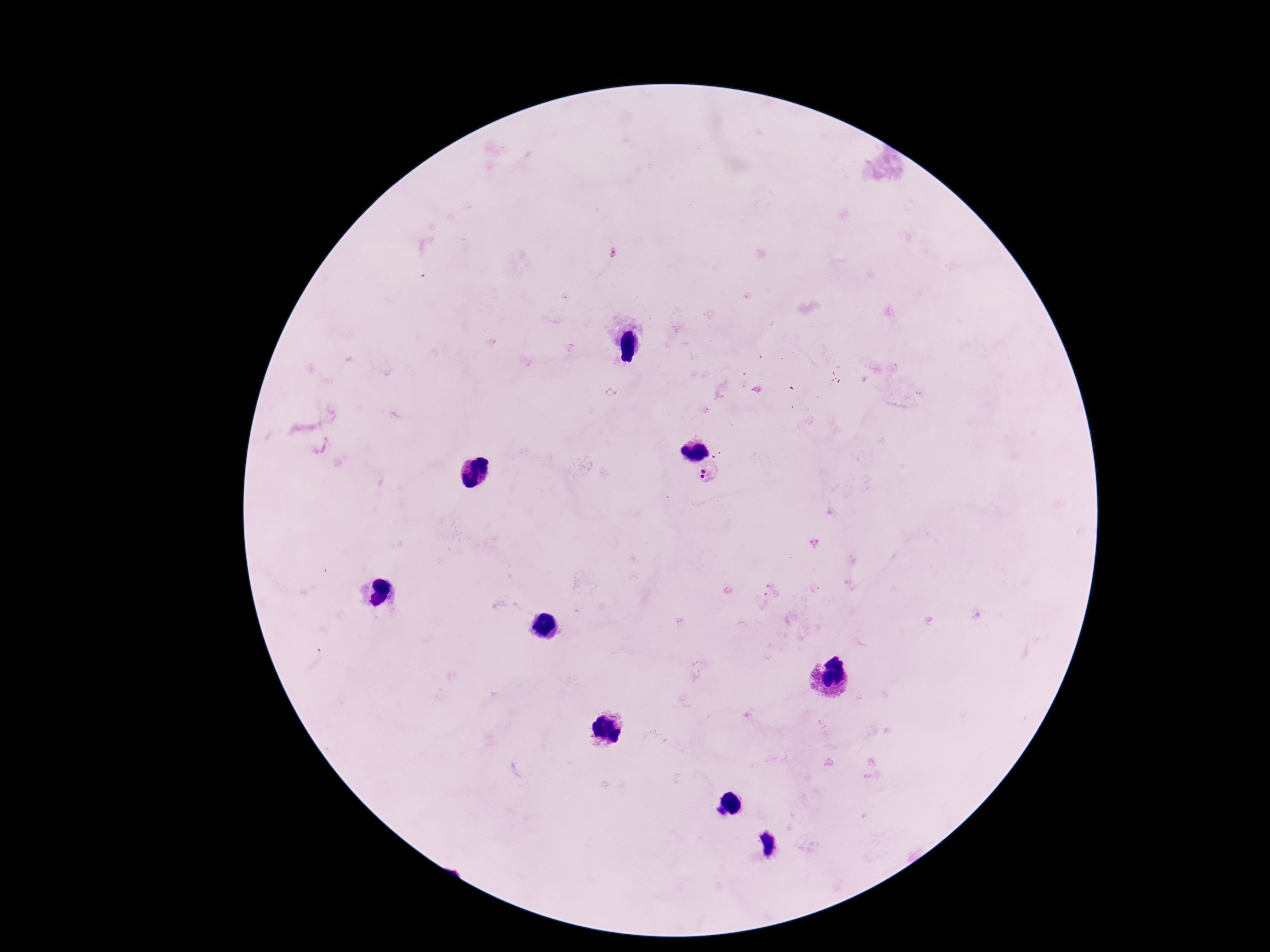
magnification = 100x
capture = smartphone camera through the microscope eyepiece
Plasmodium parasite locations = approximate object centers, in pixels from the top-left corner: (x=613, y=253), (x=707, y=473)
field of view = single
patient malaria status = positive
image size = 1270×952 pixels
preparation = thick blood smear
stain = Giemsa